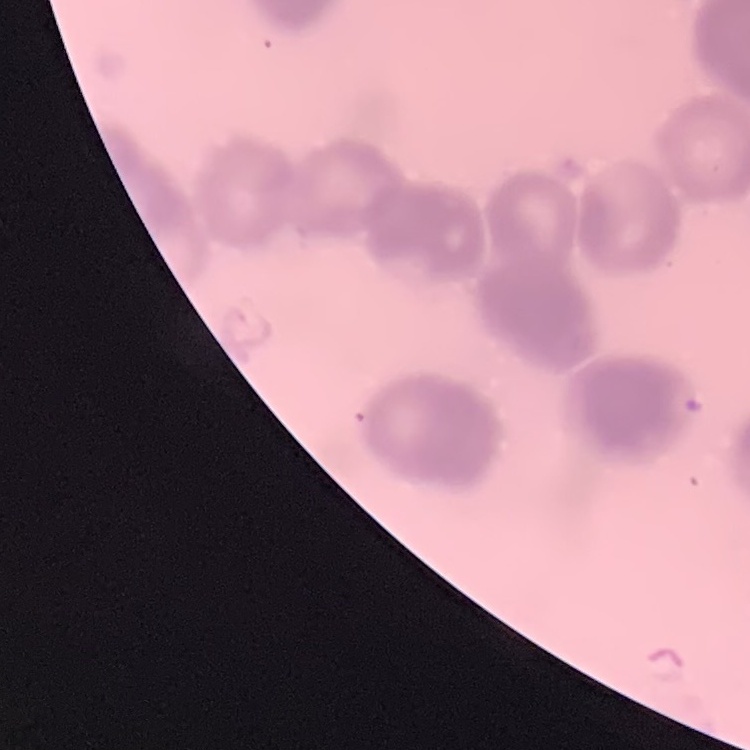
Summary:
  - Erythrocyte morphology: rouleaux formation
  - Image type: square crop of a larger photomicrograph
  - Stain: Field's or Giemsa
  - Preparation: thin blood smear